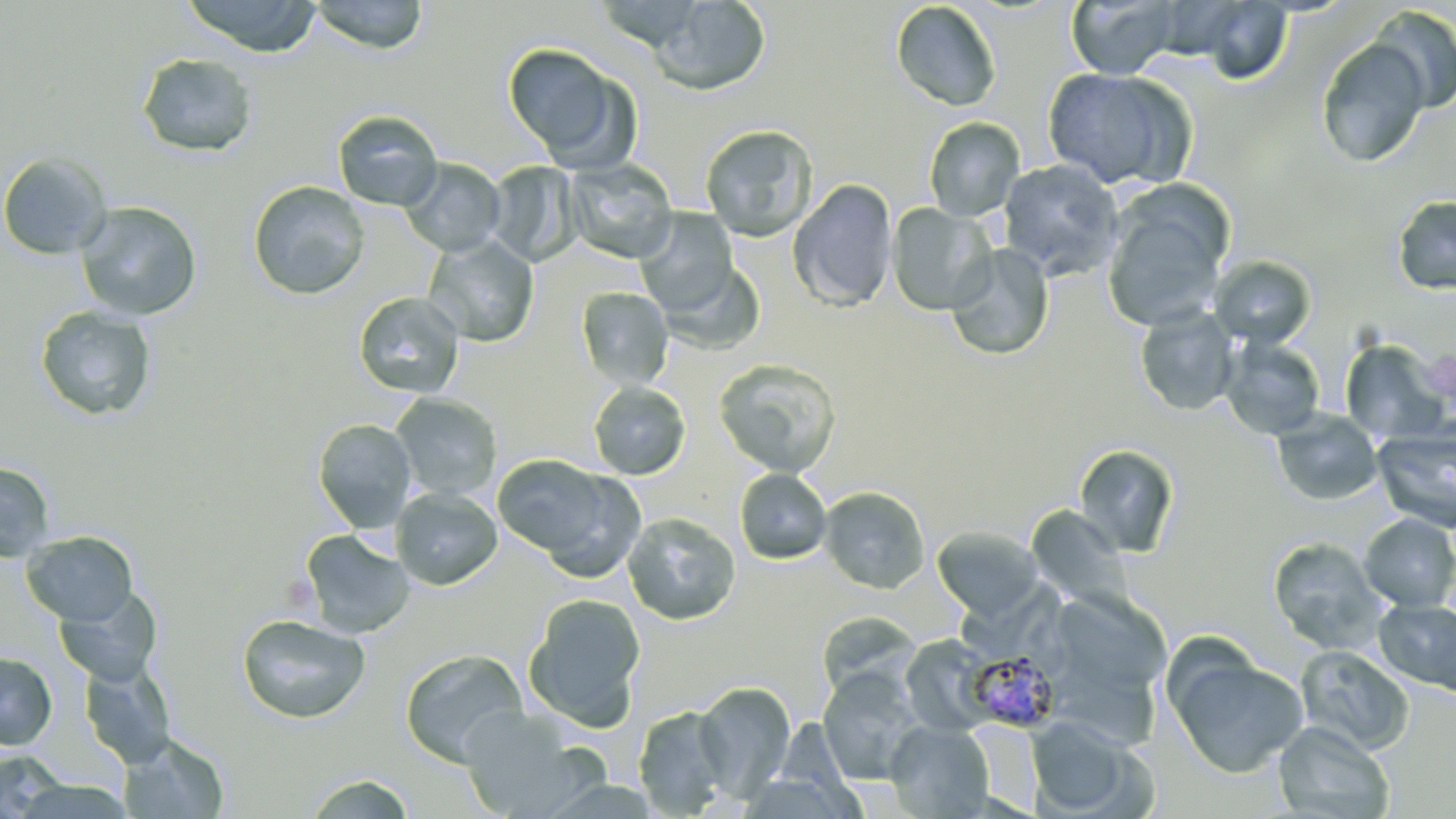

Summary:
  - Coordinate format: approximate bounding boxes as [x1, y1, x2, y2] in pixels
  - Plasmodium malariae-infected red blood cell locations: [964, 649, 1061, 732]
  - Uninfected red blood cell locations: [179, 0, 323, 57], [647, 0, 772, 96], [1066, 0, 1181, 79], [309, 1, 430, 54], [890, 1, 1002, 112], [1181, 1, 1294, 84], [1369, 6, 1456, 113], [1315, 38, 1430, 168], [501, 42, 639, 170], [136, 52, 259, 158], [1042, 67, 1194, 192], [332, 109, 443, 211], [924, 117, 1025, 221], [699, 123, 818, 241], [0, 152, 111, 260], [400, 158, 507, 257], [563, 159, 679, 264], [999, 159, 1125, 280], [485, 161, 583, 266], [787, 179, 898, 312], [247, 180, 371, 301], [1101, 186, 1232, 335], [1391, 196, 1456, 296], [74, 201, 202, 321], [886, 203, 995, 315], [635, 209, 739, 317], [422, 235, 540, 347], [945, 243, 1055, 361], [1209, 255, 1317, 349], [656, 257, 766, 356], [575, 287, 674, 391], [352, 291, 466, 400], [34, 305, 157, 422], [1134, 305, 1239, 417], [1219, 337, 1327, 439], [1339, 338, 1449, 444], [714, 358, 842, 477], [588, 381, 691, 480], [390, 393, 503, 501], [1271, 409, 1384, 506], [312, 418, 416, 533], [1372, 427, 1456, 534], [1073, 443, 1180, 558], [491, 454, 631, 570], [0, 462, 55, 562], [734, 468, 832, 564], [819, 485, 930, 594], [390, 487, 503, 590], [1025, 505, 1131, 610], [622, 512, 741, 626], [1357, 513, 1456, 611], [932, 526, 1044, 620], [299, 529, 416, 639], [21, 530, 138, 626], [1267, 536, 1390, 654], [54, 584, 164, 687], [1063, 588, 1172, 676], [523, 593, 646, 731], [1373, 598, 1456, 695], [817, 610, 921, 700], [237, 613, 371, 724], [899, 634, 997, 736], [1295, 645, 1415, 755], [1166, 646, 1309, 779], [399, 648, 528, 768], [0, 651, 57, 751], [1056, 656, 1165, 750], [78, 659, 177, 769], [817, 668, 926, 785], [694, 681, 795, 800], [457, 704, 594, 818], [633, 705, 733, 817], [1026, 716, 1137, 815], [967, 720, 1043, 810], [886, 721, 995, 819], [1272, 721, 1395, 819], [118, 734, 230, 818], [1, 750, 67, 818], [301, 774, 418, 818], [16, 779, 134, 818]
  - Slide-level diagnosis: Plasmodium malariae
  - Image size: 1456×819 pixels
  - Stain: May-Grünwald-Giemsa
  - Preparation: thin blood smear
  - Field of view: one of a larger specimen
  - Magnification: 1000x
  - Modality: light microscopy